Locate every blood parasite and identify its species.
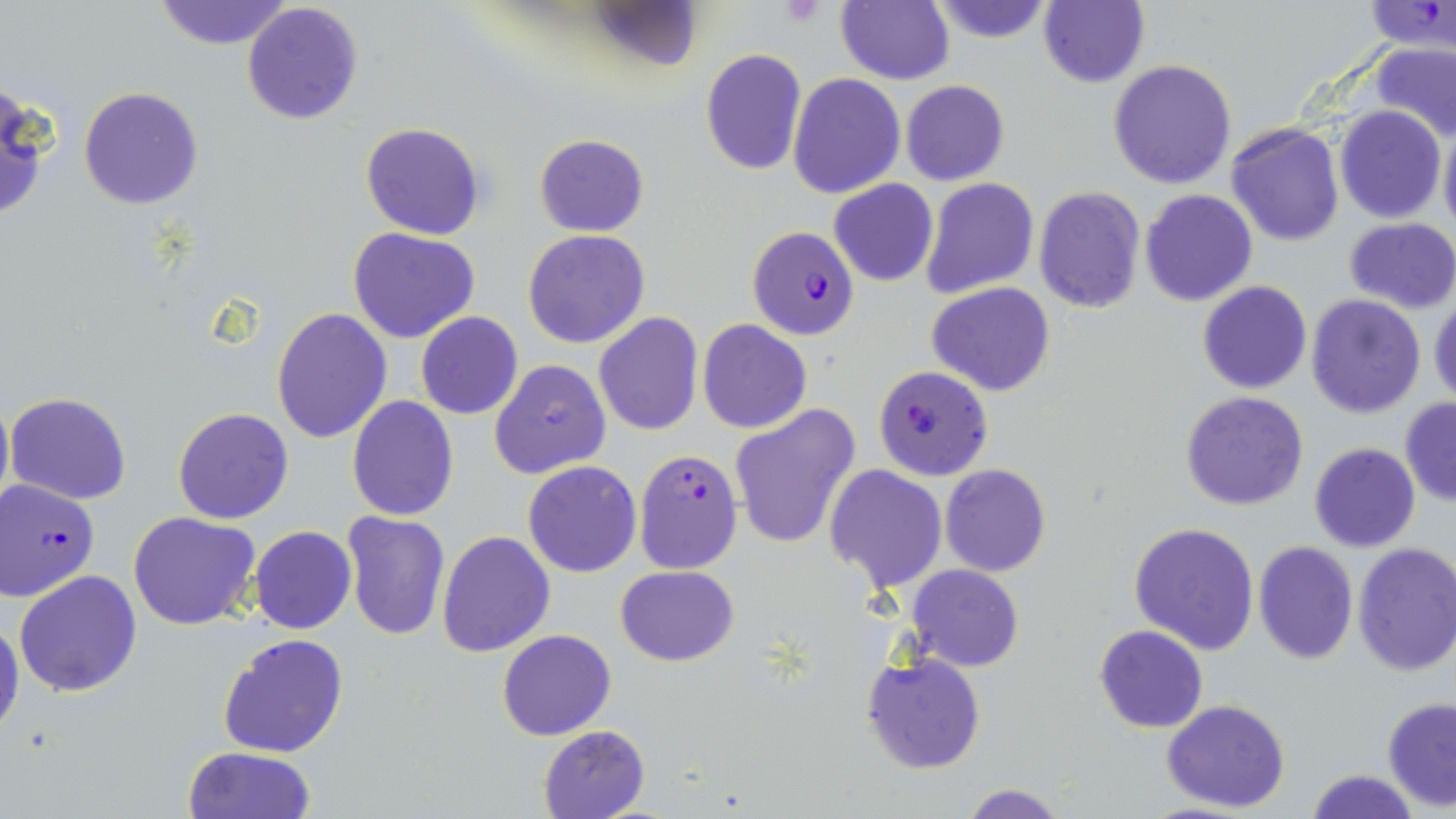

Approximate bounding boxes as (x1,y1)-(x2,y2) corner pairs in pixels.
Plasmodium falciparum-infected red blood cells (subset): (1361,1)-(1454,54), (746,225)-(860,340), (633,448)-(743,573), (0,479)-(101,602).
No Plasmodium ovale, Plasmodium malariae, Plasmodium vivax, Babesia divergens, or Trypanosoma brucei observed.

Summary:
  - Uninfected red blood cell locations (subset): (154,0)-(294,50), (594,0)-(701,72), (1040,0)-(1150,88), (835,1)-(954,84), (926,1)-(1059,45), (241,2)-(364,124), (1372,41)-(1456,142), (700,49)-(807,175), (1108,60)-(1238,189), (788,73)-(905,198), (899,80)-(1009,186), (0,84)-(51,226), (78,86)-(204,210), (1334,105)-(1446,223), (1438,121)-(1456,239), (360,122)-(486,239), (1227,123)-(1344,246), (534,133)-(649,236), (920,177)-(1037,299), (829,178)-(938,287), (1033,186)-(1144,315), (1140,189)-(1258,306), (1345,216)-(1456,313), (349,227)-(480,344), (523,229)-(651,349), (1197,280)-(1312,394), (927,282)-(1056,397), (1305,294)-(1427,419), (1429,294)-(1456,407), (272,307)-(393,444), (415,311)-(522,421), (593,312)-(704,437), (698,319)-(813,434), (489,359)-(611,479), (0,387)-(13,521), (6,391)-(131,504), (1180,391)-(1310,512), (348,395)-(459,521), (1400,397)-(1456,506), (728,403)-(862,549), (172,407)-(295,524), (1310,442)-(1421,552), (520,461)-(642,577), (939,463)-(1052,578), (823,464)-(947,592), (129,511)-(260,630), (341,512)-(451,642), (1128,520)-(1260,655), (249,525)-(357,634), (437,530)-(555,658), (1252,540)-(1359,665), (1353,543)-(1456,676), (905,564)-(1025,672), (616,565)-(740,667), (15,569)-(144,697), (0,612)-(24,745), (1094,625)-(1207,733), (497,629)-(616,739), (218,633)-(349,758), (861,650)-(985,774), (1382,696)-(1456,811), (1161,698)-(1291,813), (538,723)-(652,818), (184,746)-(316,819), (1307,770)-(1418,819), (959,783)-(1070,818)
  - Platelet locations: (779,0)-(826,27)
  - Slide-level diagnosis: Plasmodium falciparum
  - Preparation: thin blood smear
  - Image size: 1456×819 pixels
  - Field of view: single
  - Stain: May-Grünwald-Giemsa
  - Modality: optical microscopy
  - Magnification: 1000x